Assess this cell for malaria.
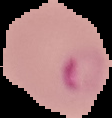
It is parasitized.

From a thin blood film. Cell region segmented out of the field of view; the surrounding area is masked to black. Image is 112×118 pixels.